Assess this cell for malaria.
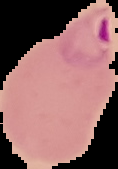

It is parasitized.

{
  "image_size": "118×169 pixels",
  "preparation": "thin blood smear",
  "image_type": "cell region segmented out of the field of view; surrounding area masked to black"
}